Locate and identify every blood parasite.
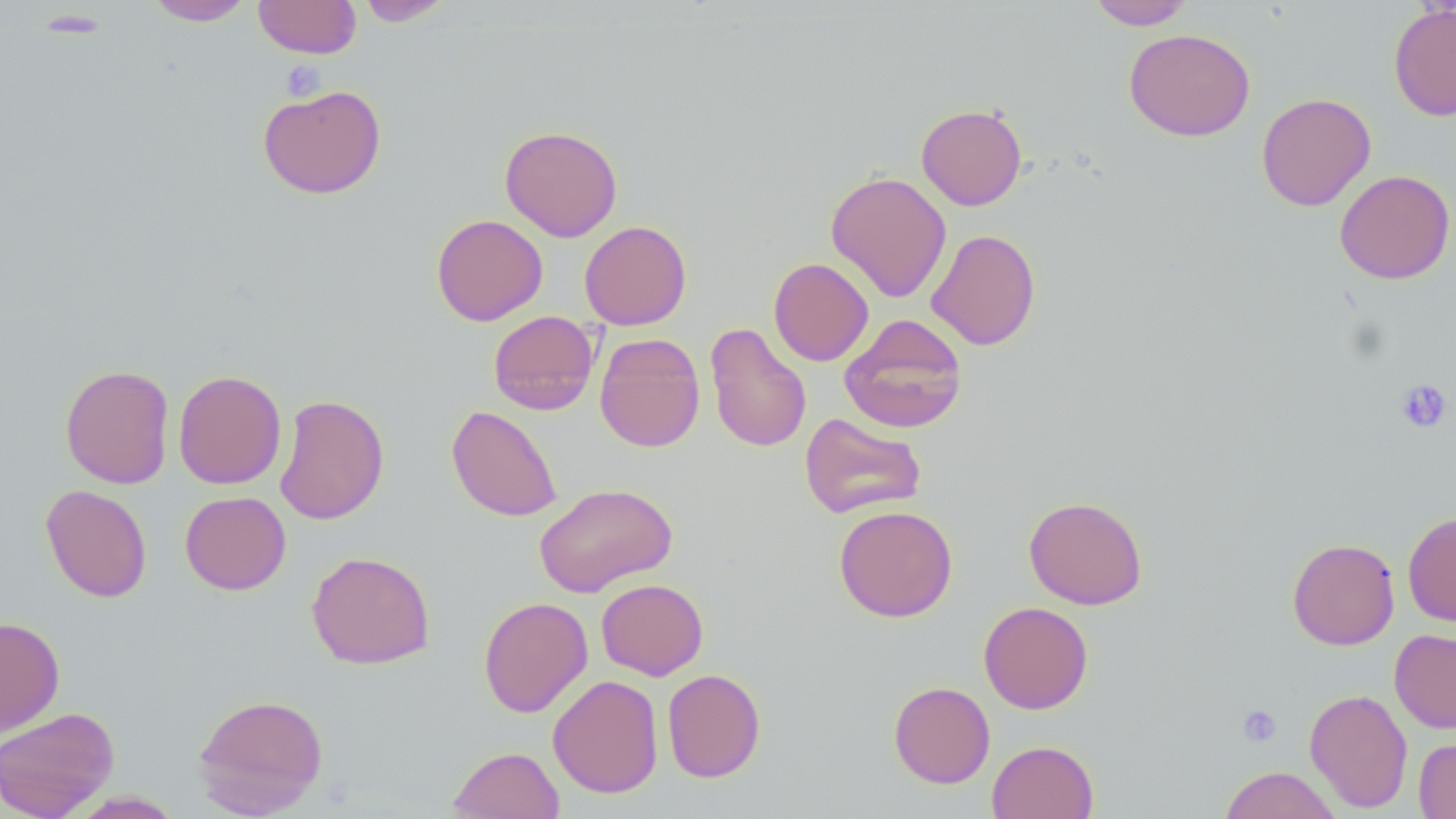
No blood parasites observed.

Summary:
  - Coordinate format: approximate bounding boxes as (x1, y1, x2, y2) in pixels
  - Platelet locations: (281, 60, 326, 99), (1395, 379, 1452, 433), (1237, 704, 1282, 747)
  - Uninfected red blood cell locations: (144, 0, 255, 26), (254, 0, 361, 58), (356, 0, 456, 26), (1086, 1, 1196, 30), (1388, 4, 1456, 121), (1124, 28, 1255, 141), (258, 84, 387, 199), (1256, 92, 1375, 211), (916, 103, 1027, 210), (499, 125, 623, 241), (1334, 169, 1455, 284), (825, 171, 952, 302), (431, 213, 548, 326), (579, 220, 691, 330), (926, 228, 1041, 350), (768, 257, 873, 366), (488, 310, 600, 415), (840, 314, 968, 434), (704, 322, 812, 454), (594, 333, 705, 453), (59, 364, 175, 489), (173, 369, 286, 489), (274, 393, 390, 525), (446, 405, 562, 522), (799, 412, 927, 519), (533, 482, 677, 597), (40, 484, 152, 602), (180, 491, 291, 595), (1023, 496, 1148, 609), (833, 504, 958, 622), (1403, 510, 1456, 627), (1287, 538, 1400, 650), (307, 550, 436, 670), (596, 578, 708, 680), (478, 596, 593, 718), (979, 601, 1093, 714), (0, 616, 65, 736), (1389, 628, 1456, 734), (662, 668, 766, 782), (548, 675, 664, 798), (888, 681, 995, 788), (1304, 687, 1413, 813), (192, 692, 329, 817), (0, 706, 120, 819), (1414, 737, 1456, 819), (987, 740, 1099, 819), (447, 746, 564, 819), (1218, 766, 1341, 819)
  - Slide-level diagnosis: negative for blood parasites
  - Field of view: single
  - Modality: optical microscopy
  - Magnification: 1000x
  - Image size: 1456×819 pixels
  - Preparation: thin blood smear
  - Stain: May-Grünwald-Giemsa